Outline each blood parasite and name the species.
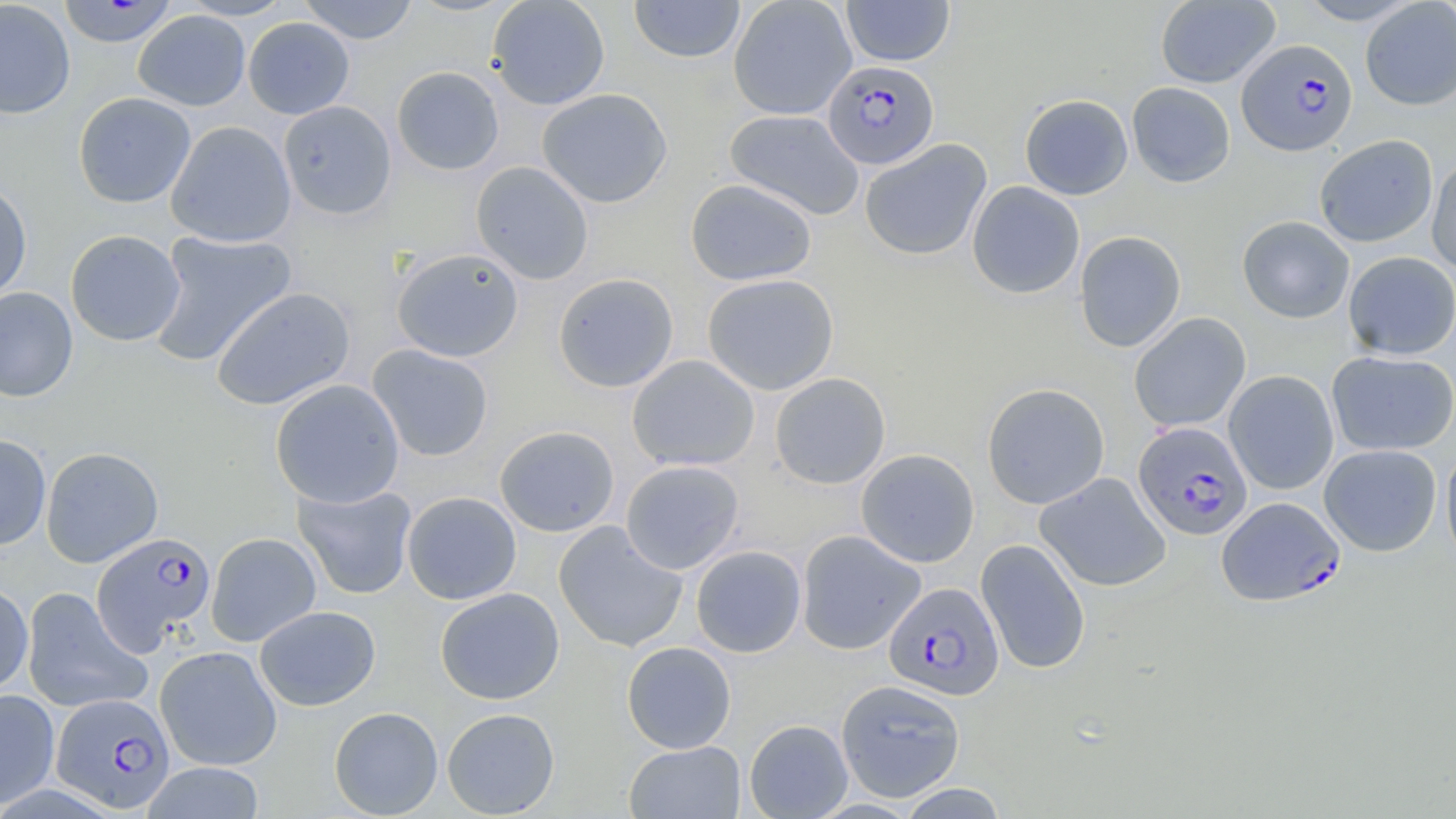
Approximate bounding boxes as [x1, y1, x2, y2] in pixels.
Plasmodium falciparum-infected red blood cells: [1237, 38, 1358, 155], [822, 59, 939, 169], [1133, 422, 1252, 540], [1216, 496, 1345, 606], [92, 532, 215, 653], [884, 582, 1004, 700], [51, 693, 174, 813].
No Plasmodium ovale, Plasmodium malariae, Plasmodium vivax, Babesia divergens, or Trypanosoma brucei observed.

Uninfected red blood cell locations: [0, 0, 75, 119], [180, 0, 297, 20], [298, 0, 418, 44], [486, 0, 610, 110], [728, 0, 856, 119], [841, 0, 955, 67], [1155, 0, 1280, 89], [1295, 0, 1422, 26], [58, 1, 178, 48], [629, 1, 746, 64], [1360, 1, 1456, 110], [133, 9, 250, 111], [243, 17, 355, 119], [391, 66, 505, 175], [1127, 82, 1235, 187], [536, 87, 673, 208], [73, 91, 196, 208], [1020, 94, 1133, 200], [278, 101, 396, 220], [724, 109, 865, 220], [166, 120, 297, 247], [1314, 134, 1438, 247], [859, 139, 992, 261], [1427, 153, 1456, 276], [470, 161, 594, 285], [685, 178, 817, 286], [0, 180, 33, 302], [967, 180, 1085, 299], [1237, 215, 1355, 323], [65, 229, 186, 346], [1074, 230, 1186, 353], [147, 231, 297, 367], [391, 248, 524, 362], [1343, 251, 1456, 360], [553, 272, 679, 393], [702, 273, 839, 395], [0, 287, 78, 401], [211, 287, 355, 410], [1129, 312, 1251, 433], [367, 344, 494, 461], [1326, 350, 1456, 455], [627, 355, 760, 471], [1224, 370, 1339, 495], [770, 372, 890, 489], [270, 379, 405, 508], [982, 383, 1110, 509], [494, 425, 620, 537], [0, 433, 51, 551], [1319, 444, 1442, 556], [41, 446, 163, 568], [1440, 446, 1456, 570], [855, 448, 979, 567], [620, 460, 744, 574], [1035, 472, 1171, 592], [293, 482, 418, 599], [402, 492, 522, 604], [554, 522, 688, 652], [796, 530, 925, 654], [206, 532, 322, 647], [976, 539, 1091, 675], [690, 545, 807, 657], [0, 581, 33, 695], [21, 587, 152, 714], [435, 587, 564, 705], [255, 605, 381, 710], [621, 641, 736, 753], [154, 646, 283, 770], [836, 679, 965, 802], [0, 688, 60, 809], [329, 706, 443, 818], [442, 708, 560, 818], [744, 719, 853, 818], [624, 741, 746, 819], [141, 762, 266, 818], [896, 783, 1009, 818]. Slide-level diagnosis: Plasmodium falciparum. Light microscopy. May-Grünwald-Giemsa stain. Thin blood film. Single field of view. Image is 1456×819 pixels. Captured at 1000x magnification.